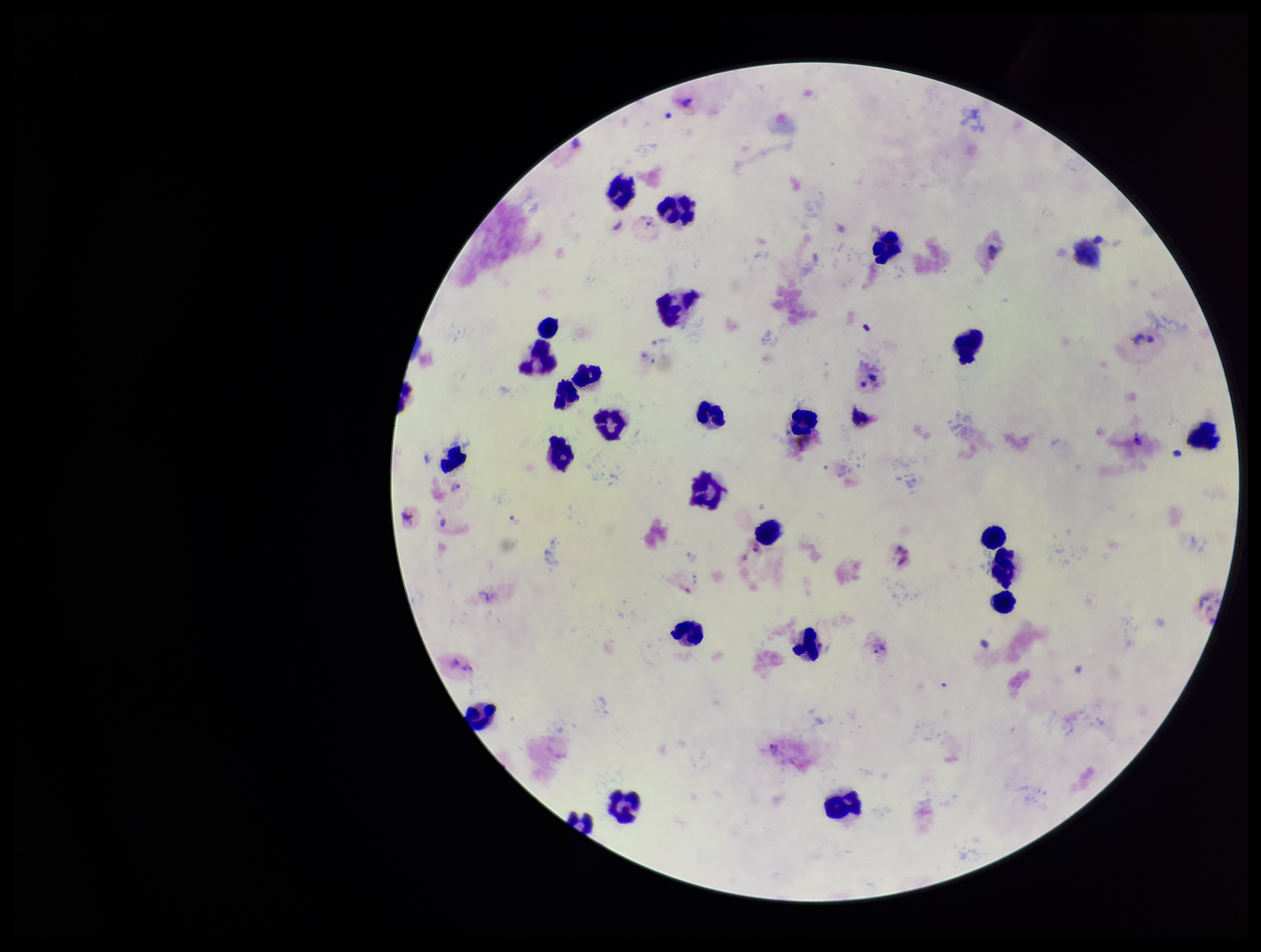

Leukocyte count: 27. Image is 1261×952 pixels. Patient malaria status: positive. Species reported for this patient: Plasmodium vivax. Single field of view. Photographed through the microscope eyepiece with a smartphone camera. Plasmodium parasites: identified. Parasite count: 4. Stained with Giemsa. Preparation: thick smear.